Classify this cell by malaria status.
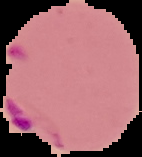
Parasitized.

image_size: 142×157 pixels
image_type: cell region segmented out of the field of view; surrounding area masked to black
preparation: thin blood film